Report the malaria status of this cell.
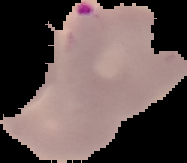

It is parasitized.

Image is 187×163 pixels. Segmented cell region on a black background. From a thin blood film.